Identify the parasite.
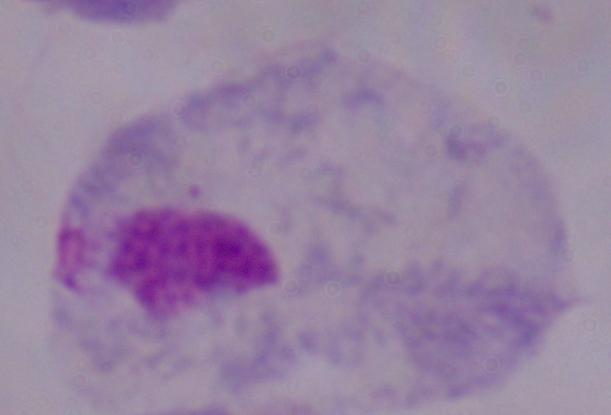
This is a trichomonad.

Summary:
  - Magnification: 1000x
  - Modality: micrograph